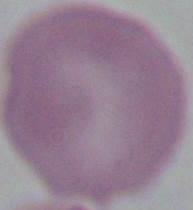
Summary:
  - Magnification: 1000x
  - Identification: erythrocyte
  - Modality: photomicrograph